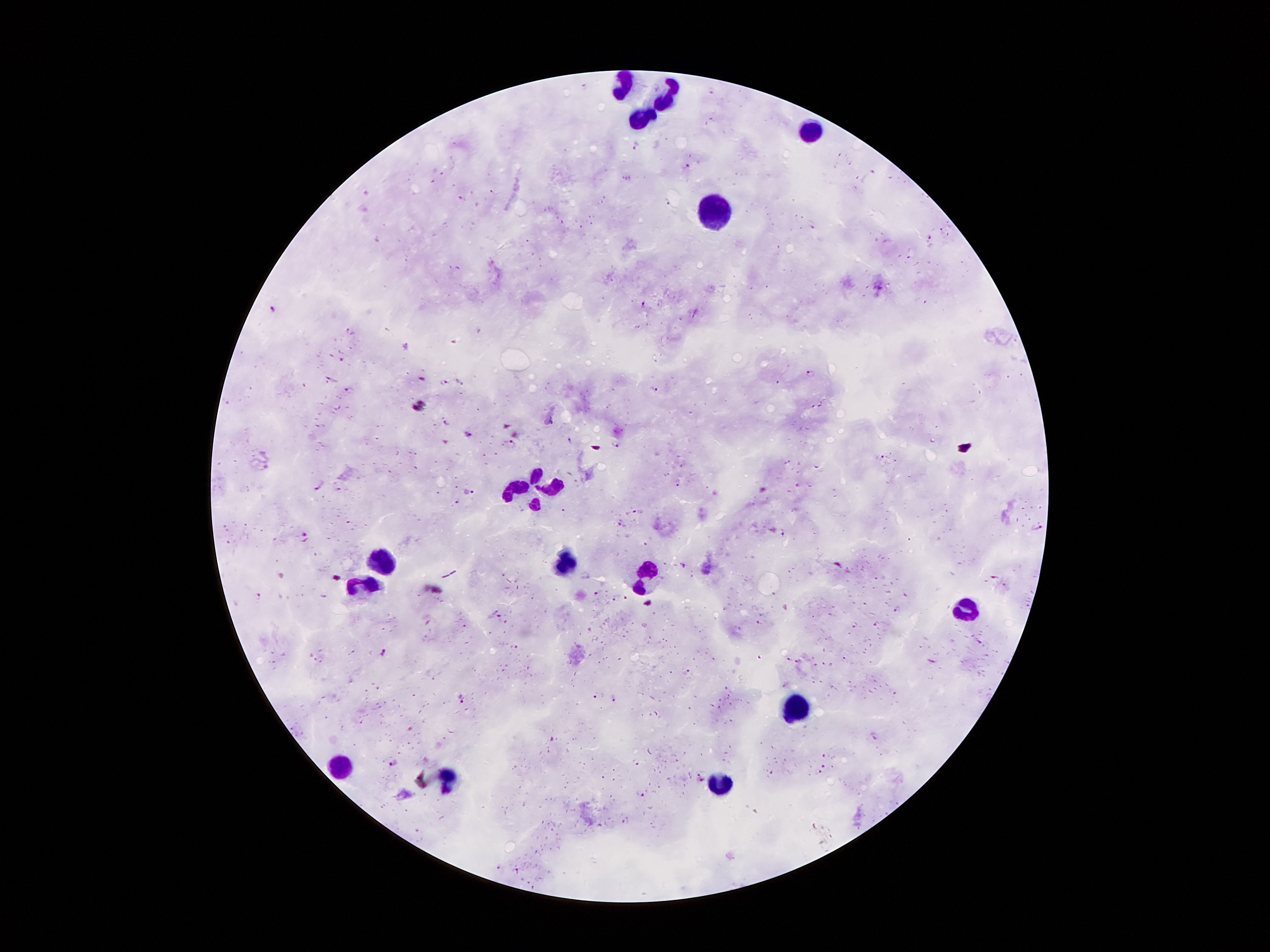
Approximate centers as (x, y) in pixels.
Summary:
  - Malaria parasite locations: (585, 86), (711, 91), (635, 143), (685, 165), (870, 176), (463, 198), (667, 202), (813, 227), (941, 231), (928, 237), (643, 305), (274, 309), (349, 329), (454, 341), (343, 360), (811, 374), (332, 380), (445, 383), (349, 389), (654, 390), (821, 405), (447, 423), (466, 434), (570, 440), (511, 444), (615, 446), (880, 458), (818, 466), (677, 483), (321, 486), (339, 490), (469, 492), (458, 502), (637, 512), (620, 524), (1038, 527), (783, 533), (305, 534), (685, 567), (995, 578), (1004, 584), (598, 591), (258, 594), (615, 600), (498, 617), (759, 623), (855, 625), (464, 627), (981, 642), (516, 648), (384, 651), (788, 659), (844, 659), (932, 660), (797, 661), (688, 672), (462, 698), (594, 698), (613, 700), (874, 736), (824, 756), (394, 764), (824, 766), (816, 773), (699, 775), (702, 781), (641, 794), (626, 821), (498, 868), (516, 870)
  - Leukocyte locations: (620, 84), (667, 96), (637, 115), (812, 130), (713, 209), (548, 482), (521, 492), (380, 558), (563, 563), (644, 577), (365, 590), (963, 608), (798, 708), (338, 765), (447, 775), (718, 787)
  - Image size: 1270×952 pixels
  - Stain: Giemsa
  - Capture: smartphone through the microscope eyepiece
  - Field of view: one from this slide
  - Preparation: thick blood film
  - Magnification: 100x
  - Patient malaria status: infected with Plasmodium falciparum